Classify this cell by malaria status.
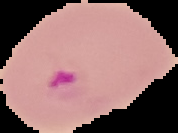
Parasitized.

Summary:
  - Image type: segmented cell region on a black background
  - Preparation: thin blood smear
  - Image size: 178×133 pixels